Give the position of every malaria parasite.
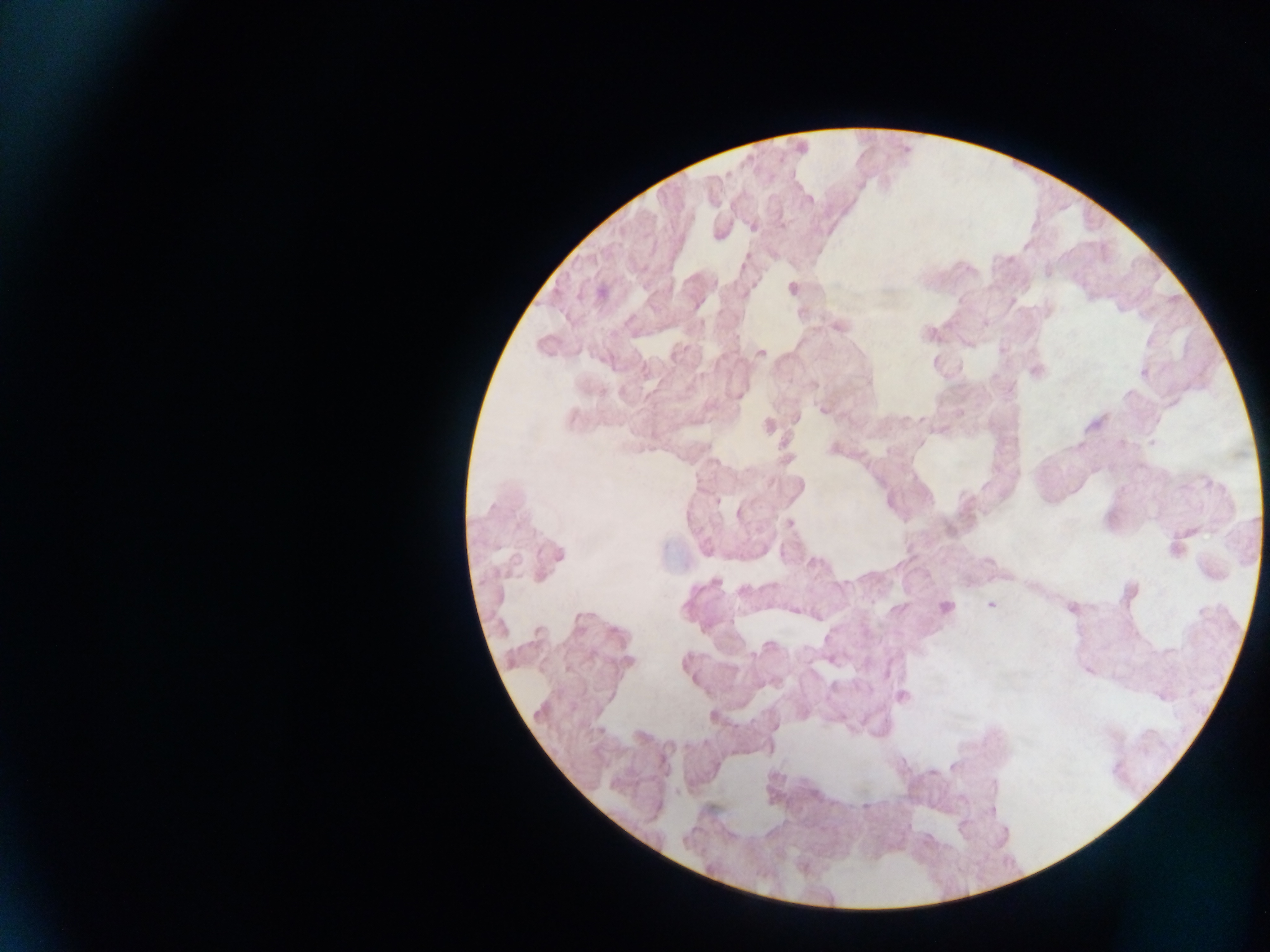
Approximate centers as x y in pixels.
Malaria parasites: 790 523; 990 604; 946 606.

Summary:
  - Field of view: single
  - Preparation: thick blood smear
  - Image size: 1270×952 pixels
  - Country: Ghana
  - Capture: mobile-phone photograph through a microscope